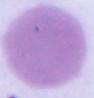

A red blood cell is seen. Photomicrograph. Captured at 1000x magnification.